Name the parasite shown.
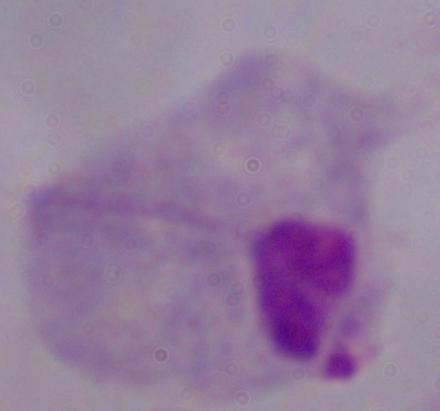
This is a trichomonad.

{
  "modality": "micrograph",
  "magnification": "1000x"
}